Assess the morphology of the red blood cells.
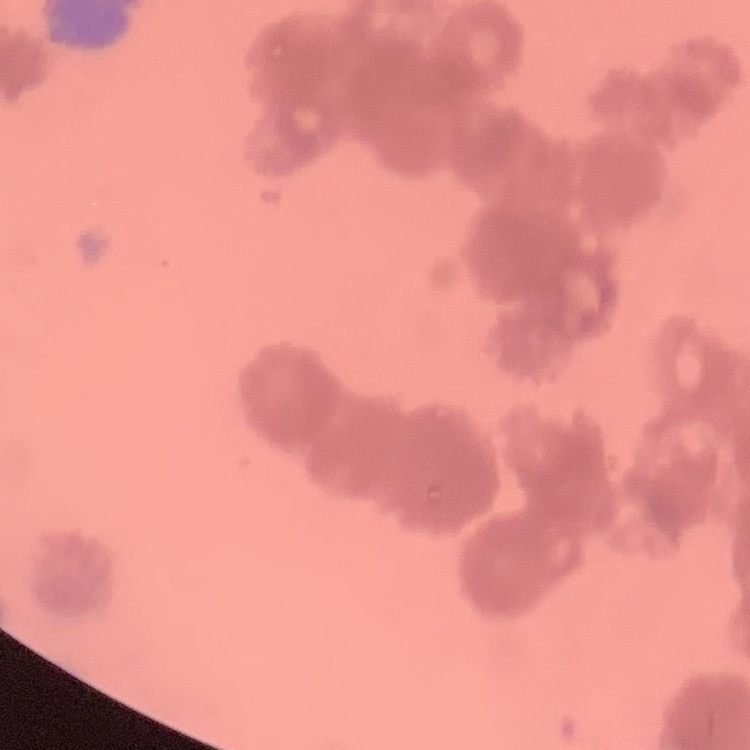

Rouleaux formation.

Summary:
  - Preparation: thin blood film
  - Image type: square crop of a larger photomicrograph
  - Stain: Field's or Giemsa